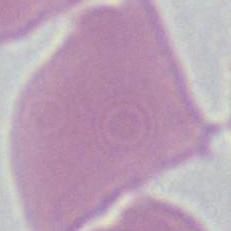
identification = red blood cell
modality = micrograph
magnification = 1000x